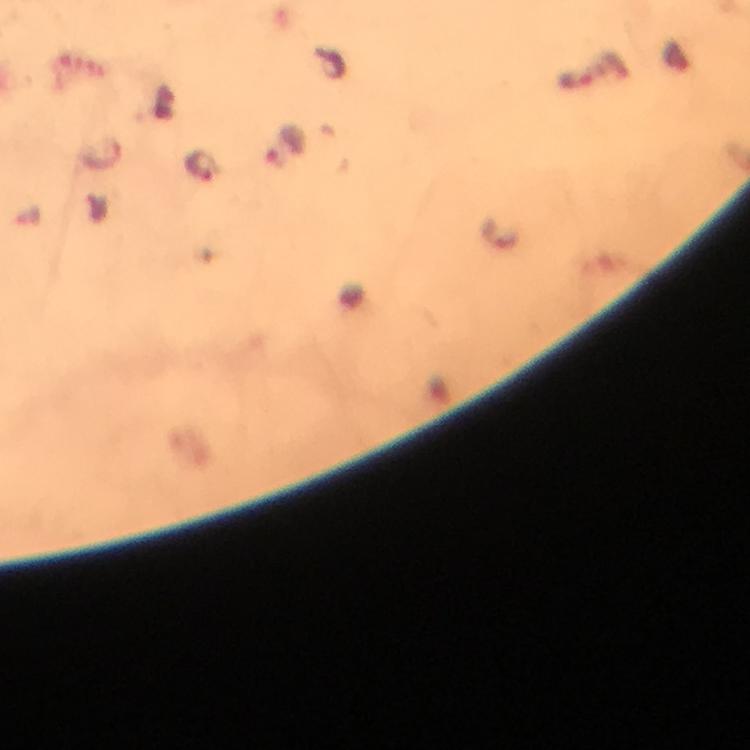
Approximate object centers, in pixels from the top-left corner.
Summary:
  - Malaria parasite locations: (x=286, y=145), (x=199, y=166)
  - Image size: 750×750 pixels
  - Capture: smartphone camera through the microscope
  - Magnification: 100x
  - Preparation: thick blood film
  - Immersion oil: used
  - Context: from a malaria diagnostic workup
  - Cropped from: a single field of view
  - Stain: Giemsa